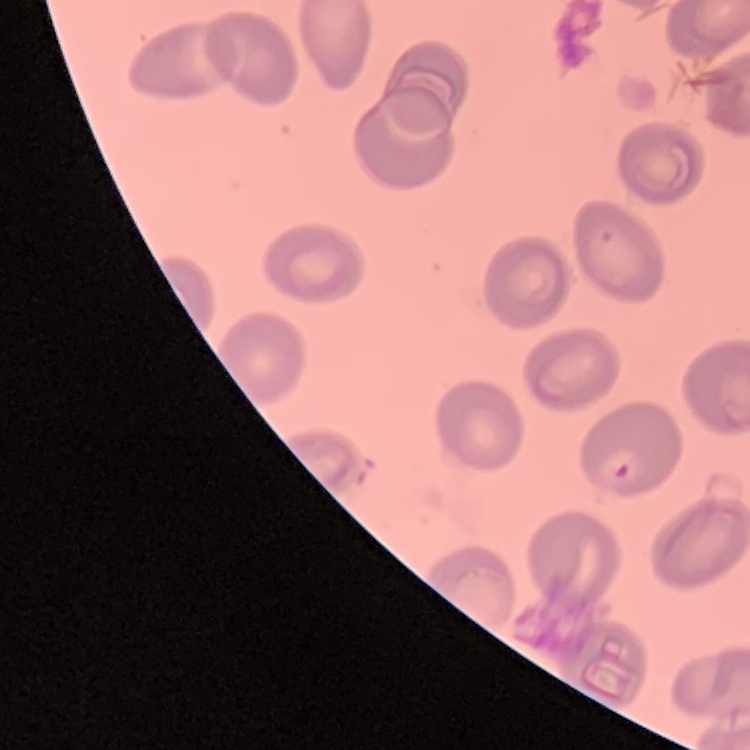
red blood cell morphology = no rouleaux formation
image type = one tile cut from a larger photomicrograph
preparation = thin peripheral smear
stain = Field's or Giemsa